Point out each Plasmodium parasite.
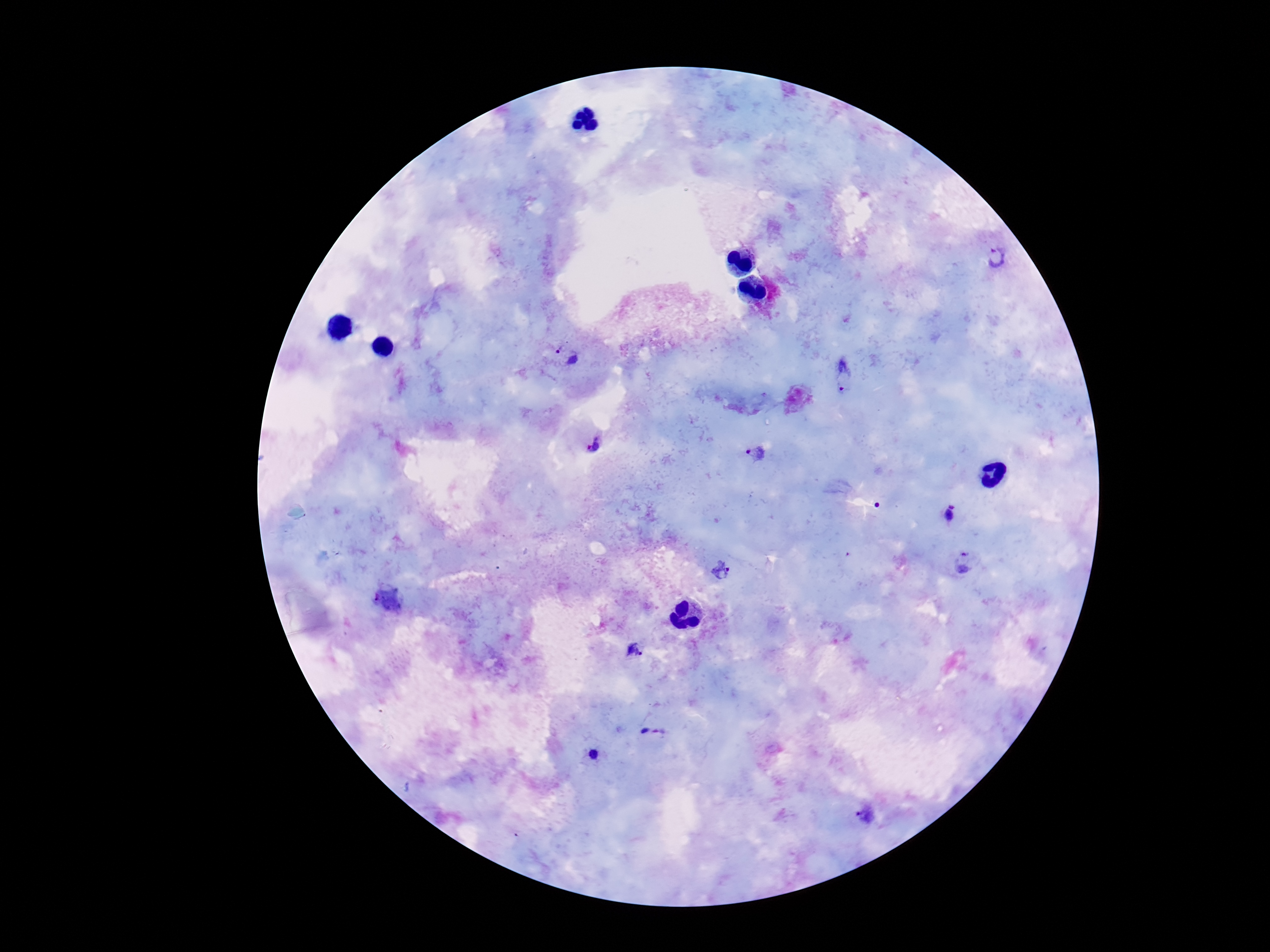
Approximate centers as [x, y] in pixels.
Plasmodium parasites: [997, 258], [566, 354], [843, 378], [590, 438], [757, 453], [949, 514], [964, 562], [723, 570], [390, 599], [636, 652], [652, 731], [593, 753], [866, 815].

Summary:
  - Field of view: single
  - Capture: smartphone camera through the microscope eyepiece
  - Preparation: thick peripheral-blood smear
  - Magnification: 100x
  - Stain: Giemsa
  - Patient malaria status: positive
  - Image size: 1270×952 pixels